Locate every Plasmodium parasite.
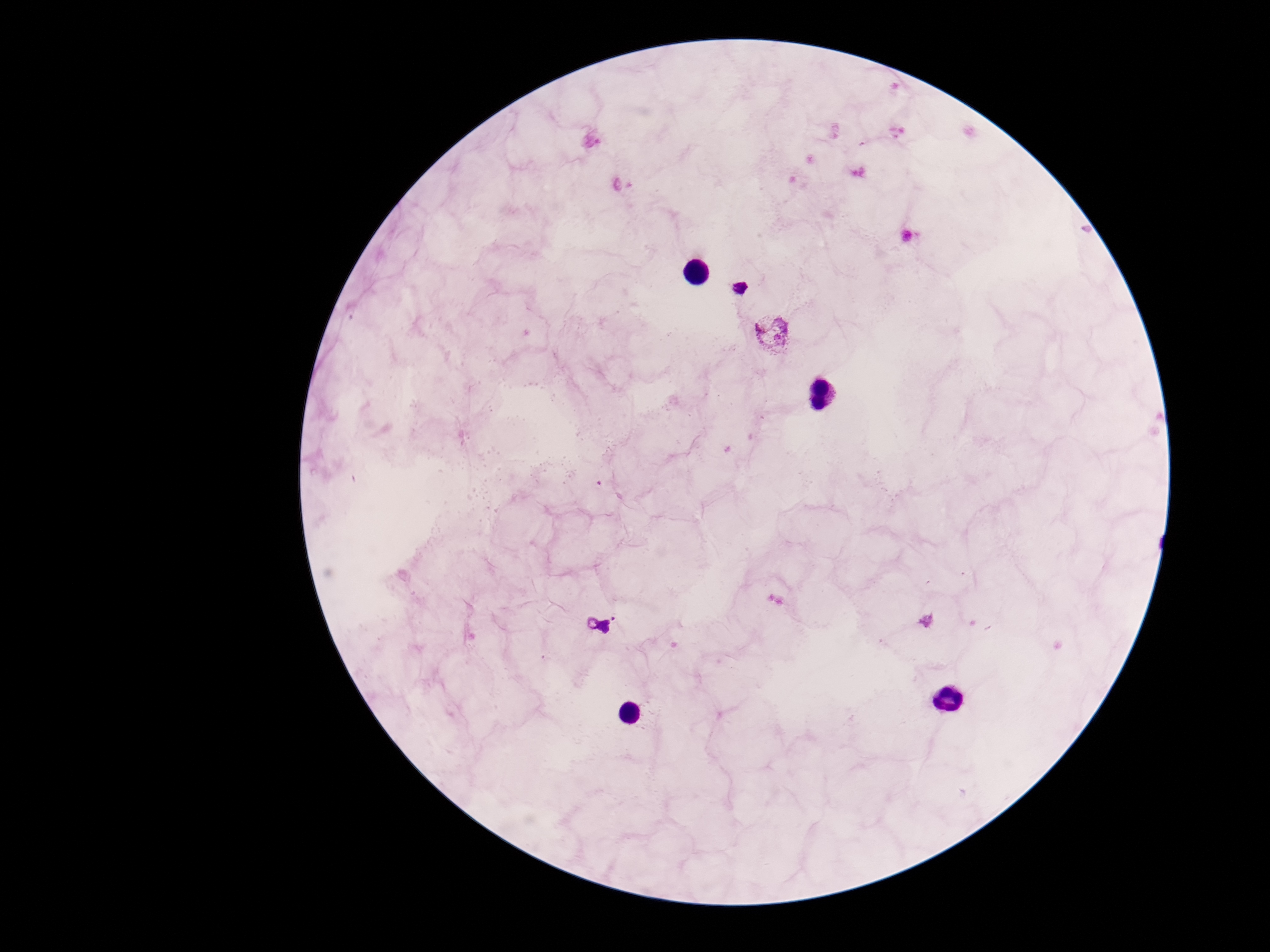

Approximate centers as {x, y} in pixels.
Plasmodium parasites: {738, 287}, {772, 333}, {598, 624}.

patient malaria status = positive
stain = Giemsa
field of view = single
capture = smartphone camera through the microscope eyepiece
preparation = thick blood smear
image size = 1270×952 pixels
magnification = 100x